Give the position of every leukocyte visible.
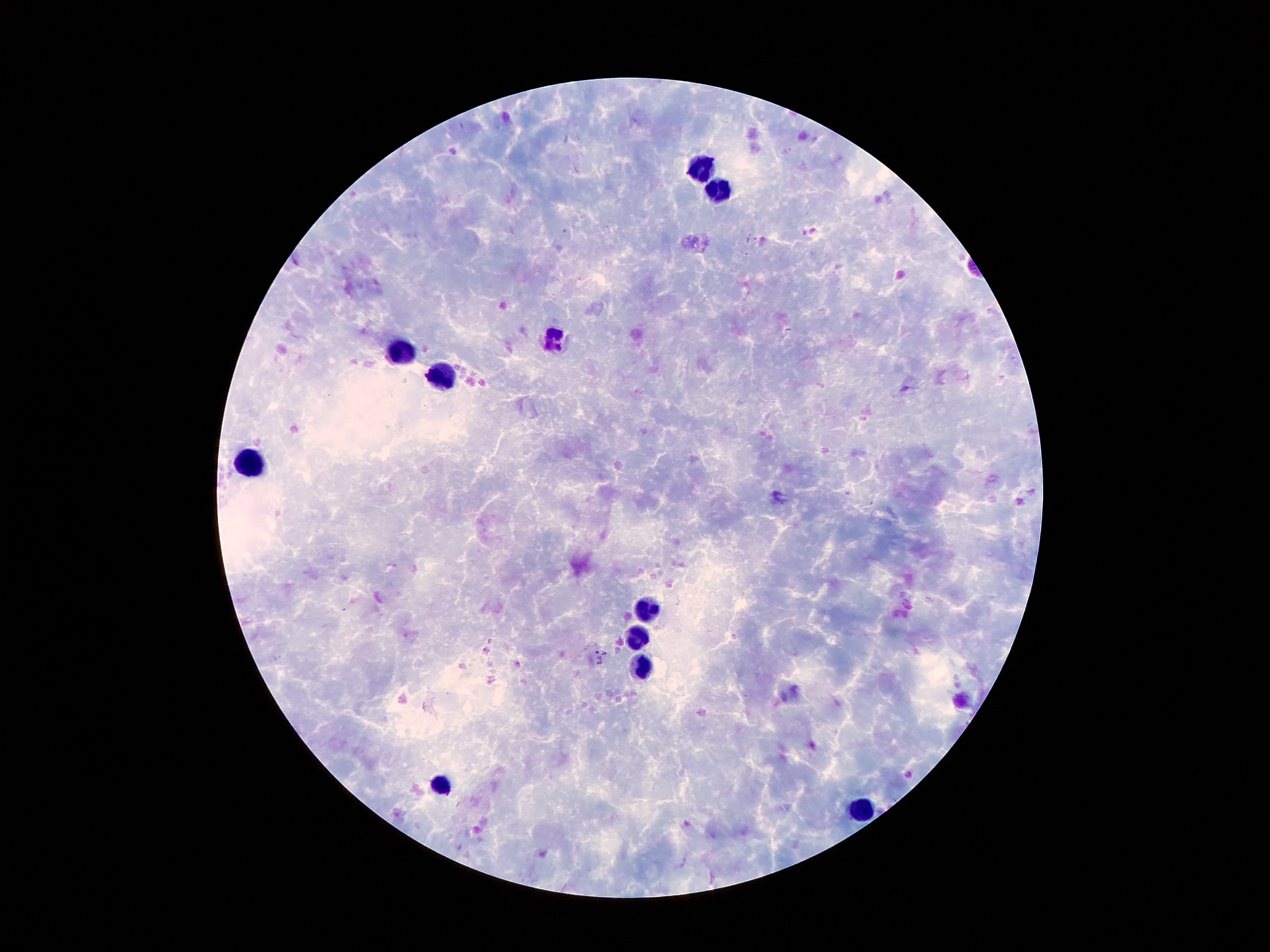

Approximate object centers, in pixels from the top-left corner.
Leukocytes: (x=702, y=164), (x=724, y=188), (x=555, y=338), (x=403, y=351), (x=447, y=376), (x=247, y=455), (x=650, y=606), (x=640, y=635), (x=642, y=667), (x=444, y=785), (x=865, y=810).

malaria parasite locations = (x=596, y=653), (x=604, y=653), (x=600, y=662)
capture = smartphone through the microscope eyepiece
patient malaria status = positive for Plasmodium falciparum
stain = Giemsa
magnification = 100x
image size = 1270×952 pixels
field of view = one from this slide
preparation = thick peripheral-blood smear